Classify this cell by malaria status.
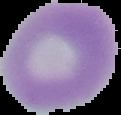
It is uninfected.

Summary:
  - Preparation: thin blood film
  - Image type: cell region segmented out of the field of view; surrounding area masked to black
  - Image size: 121×115 pixels